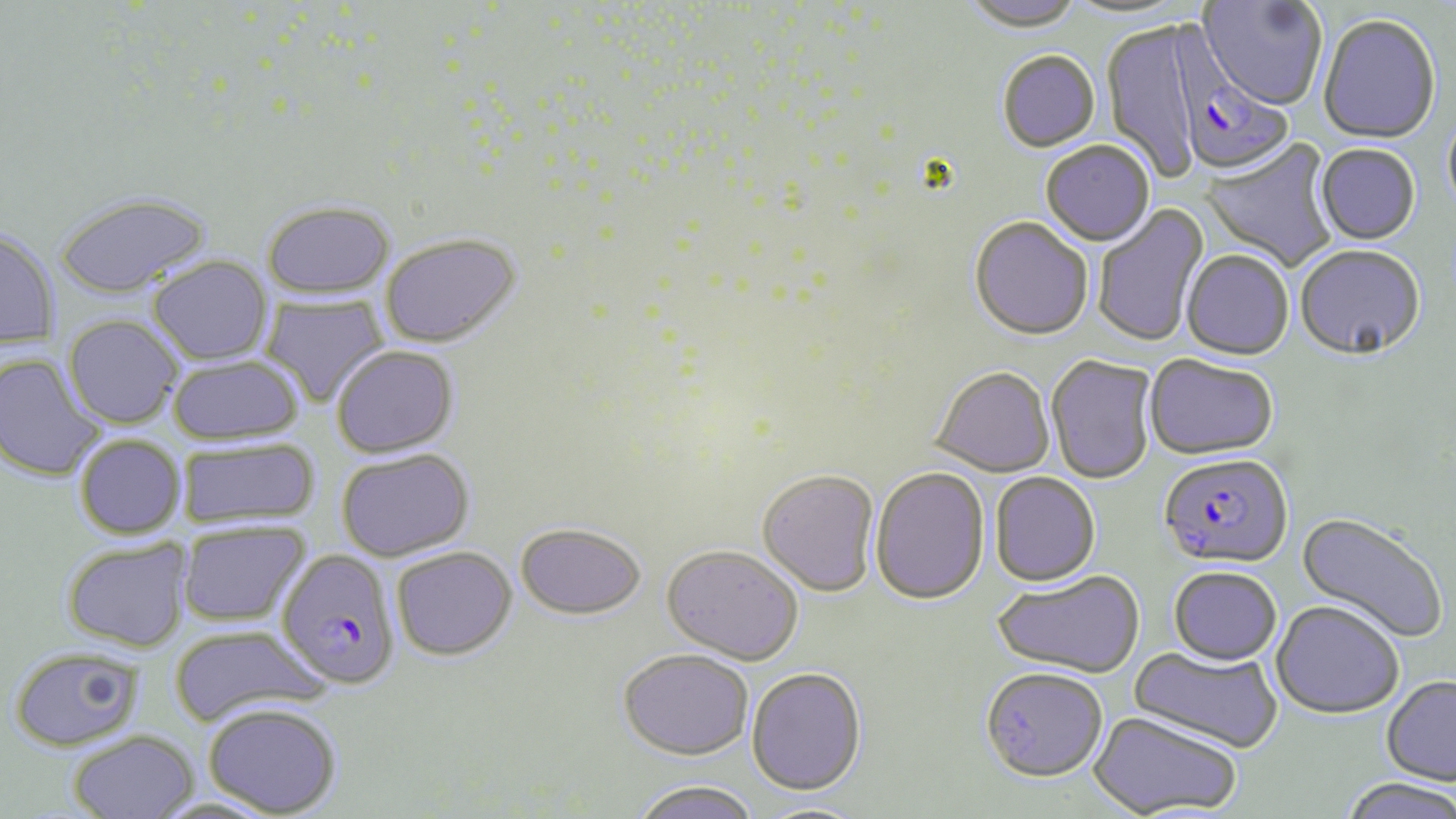
Approximate bounding boxes as [x1, y1, x2, y2] in pixels. Uninfected red blood cell locations: [960, 0, 1083, 35], [1059, 0, 1195, 22], [1198, 0, 1327, 112], [1318, 17, 1441, 146], [1102, 21, 1204, 182], [997, 53, 1100, 154], [1442, 108, 1456, 226], [1200, 138, 1339, 272], [1040, 143, 1155, 248], [1314, 145, 1421, 247], [53, 192, 213, 299], [261, 200, 395, 298], [1092, 202, 1210, 347], [969, 219, 1093, 343], [0, 228, 60, 350], [380, 233, 522, 348], [1295, 247, 1425, 365], [1181, 252, 1294, 362], [147, 255, 274, 365], [259, 295, 390, 408], [63, 315, 184, 428], [331, 345, 459, 457], [0, 353, 108, 482], [168, 355, 303, 445], [1046, 356, 1157, 485], [1144, 356, 1278, 462], [929, 369, 1056, 479], [75, 434, 187, 539], [177, 439, 320, 527], [336, 448, 475, 561], [870, 469, 989, 607], [757, 470, 880, 598], [990, 474, 1101, 588], [1294, 511, 1448, 645], [177, 521, 311, 626], [514, 522, 646, 619], [61, 538, 193, 653], [661, 544, 804, 665], [391, 546, 516, 660], [1169, 569, 1281, 669], [992, 571, 1145, 681], [1271, 603, 1404, 721], [169, 625, 327, 728], [8, 645, 145, 751], [1127, 645, 1283, 756], [617, 649, 754, 761], [746, 669, 867, 798], [981, 671, 1108, 785], [1381, 678, 1456, 788], [201, 702, 344, 817], [1088, 712, 1242, 818], [67, 730, 200, 818], [1337, 779, 1456, 819], [630, 780, 762, 819], [754, 802, 872, 819]. Plasmodium falciparum-infected red blood cell locations: [1173, 43, 1295, 180], [1159, 456, 1294, 573], [276, 549, 401, 689]. Slide-level diagnosis: Plasmodium falciparum. Light microscopy. 1000x magnification. Single field of view. Thin blood smear. May-Grünwald-Giemsa-stained preparation. Image is 1456×819 pixels.